Assess this cell for malaria.
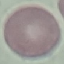
Uninfected.

Thin smear of blood. Acquired by smartphone through the microscope eyepiece. Giemsa stain. Cell patch, automatically extracted from a larger field of view and resized to 64 × 64 pixels.